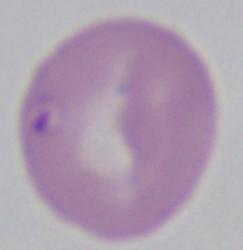

{
  "magnification": "1000x",
  "modality": "micrograph",
  "identification": "Babesia"
}